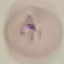

Summary:
  - Malaria status: parasitized
  - Stain: Giemsa
  - Capture: smartphone camera at the microscope eyepiece
  - Image type: automatically extracted cell patch, resized to 64 × 64 pixels
  - Preparation: thin blood film